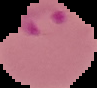

From a thin blood smear. The area outside the segmented cell region is set to black. Malaria status: parasitized. Image is 97×88 pixels.